Name the parasite shown.
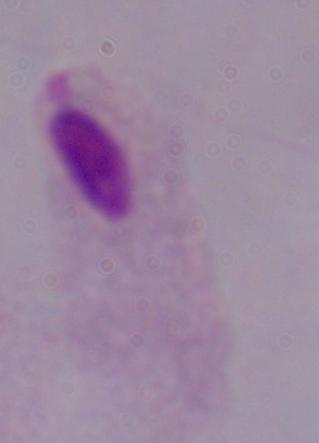
This is a trichomonad.

Summary:
  - Modality: micrograph
  - Magnification: 1000x